Point out each Plasmodium parasite.
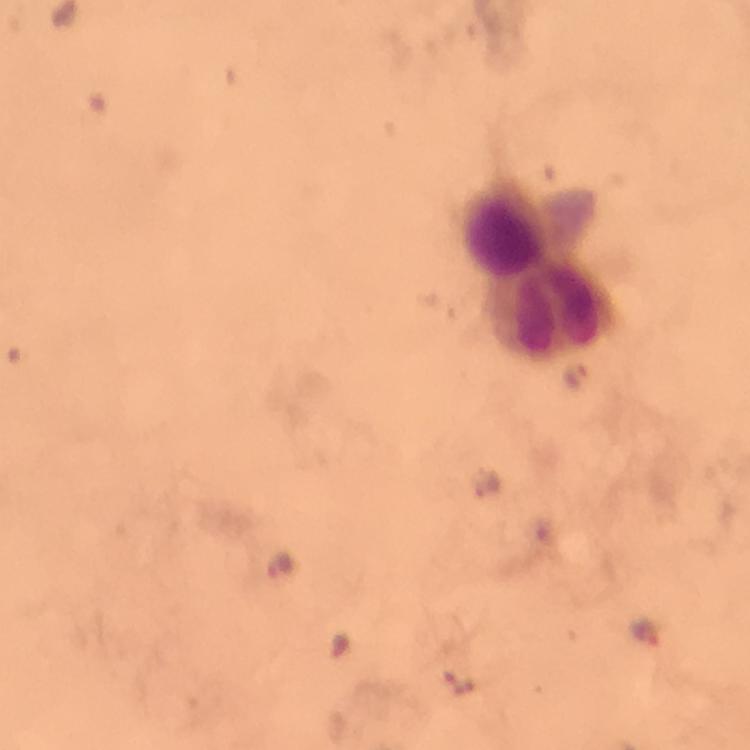

Approximate centers as (x, y) in pixels.
Plasmodium parasites: (573, 378), (281, 566), (647, 633).

context = from a malaria diagnostic workup
stain = Giemsa
immersion oil = applied
capture = smartphone mounted on the microscope
leukocyte locations = approximate centers as (x, y) in pixels: (536, 268)
preparation = thick smear
image size = 750×750 pixels
magnification = 100x
cropped from = one field of view